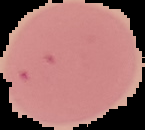 Segmented cell region on a black background. Result: no malaria parasites seen. Image is 145×130 pixels. From a thin blood film.